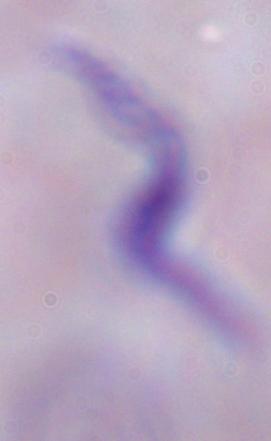
A trypanosome is shown. 1000x magnification. Photomicrograph.